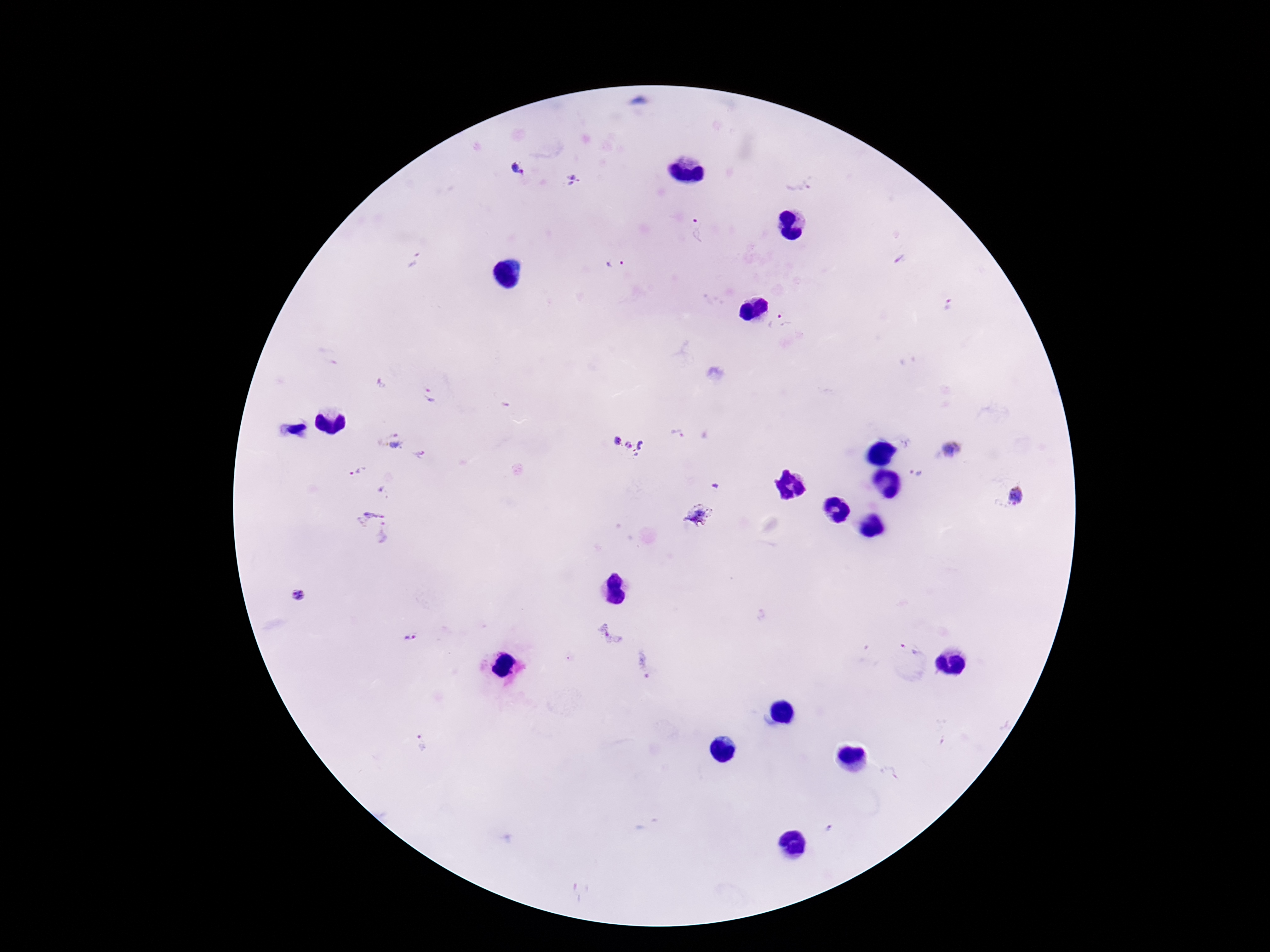
image_size: 1270×952 pixels
preparation: thick blood smear
capture: smartphone camera through the microscope eyepiece
magnification: 100x
field_of_view: one from this slide
stain: Giemsa
plasmodium_parasite_locations: 'approximate centers as [x, y] in pixels: [518, 169], [575, 180], [799, 180], [701, 230], [900, 259], [415, 261], [616, 265], [947, 305], [779, 326], [431, 395], [674, 435], [630, 437], [391, 444], [954, 448], [421, 455], [359, 472], [916, 474], [714, 486], [385, 493], [1016, 496], [701, 516], [375, 525], [298, 596], [609, 632], [410, 638], [909, 649], [644, 661], [420, 748], [890, 772], [828, 830]'
patient_malaria_status: positive